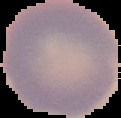

Image is 121×118 pixels. Result: no Plasmodium parasites detected. From a thin blood film. The area outside the segmented cell region is set to black.